State which parasite is depicted.
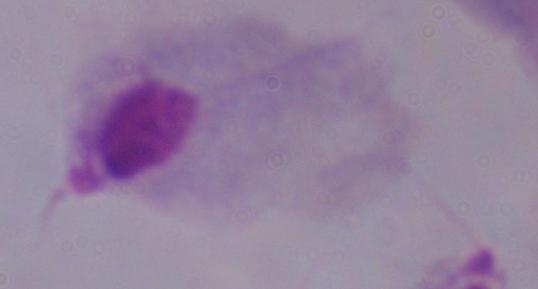

A trichomonad.

Captured at 1000x magnification. Photomicrograph.